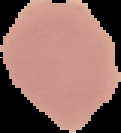
Summary:
  - Image type: segmented cell region on a black background
  - Preparation: thin blood film
  - Image size: 121×133 pixels
  - Result: no malaria parasites detected